Report the malaria status of this cell.
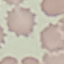

It is uninfected.

Summary:
  - Capture: smartphone through the microscope eyepiece
  - Stain: Giemsa
  - Preparation: thin blood smear
  - Image type: cell patch, automatically extracted from a larger field of view and resized to 64 × 64 pixels